Assess the morphology of the erythrocytes.
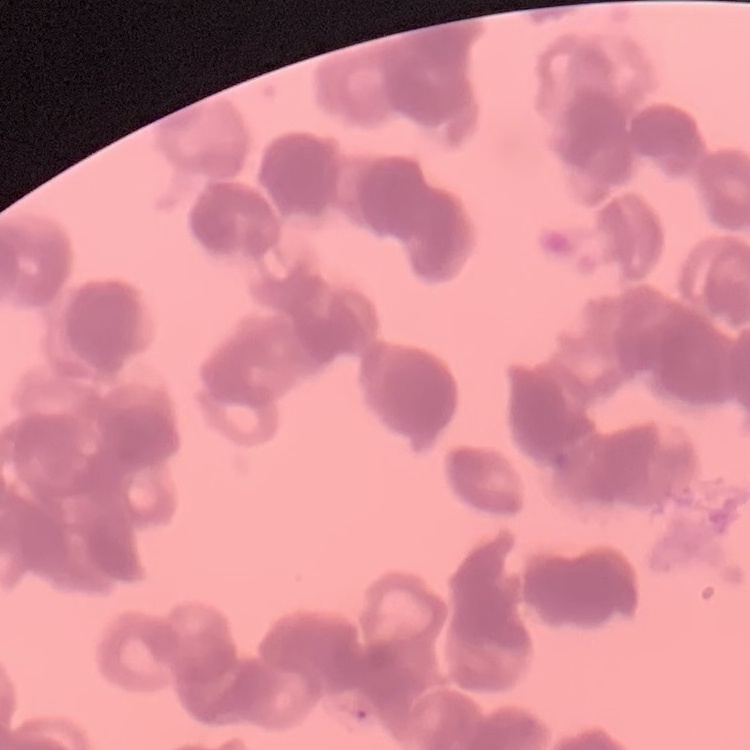

They show rouleaux formation.

Field's or Giemsa stain. One tile cut from a larger photomicrograph. Thin blood smear.